Describe the morphology of the red blood cells.
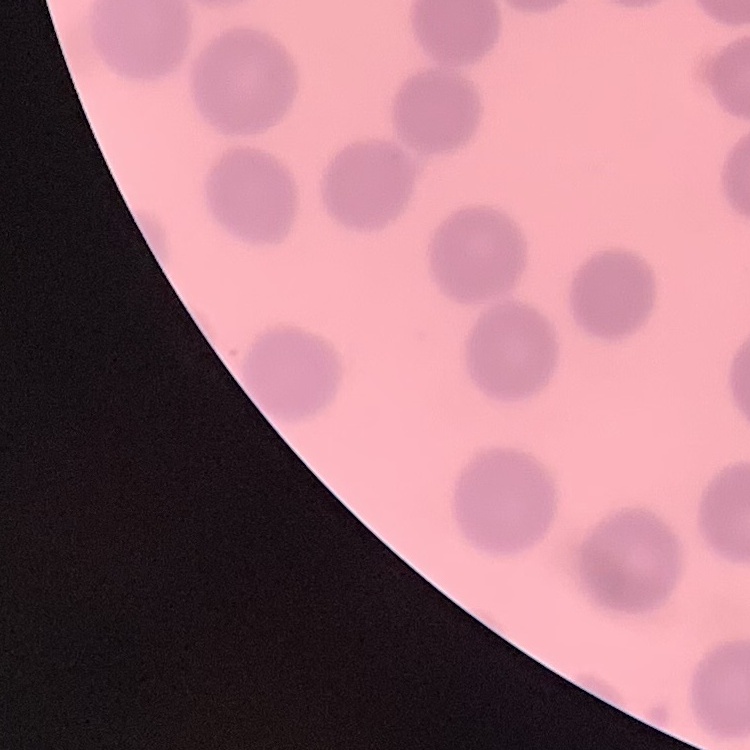

No rouleaux formation.

preparation = thin blood smear
stain = Field's or Giemsa
image type = square crop of a larger photomicrograph